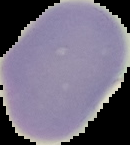
Summary:
  - Malaria status: uninfected
  - Image type: segmented cell region on a black background
  - Image size: 130×145 pixels
  - Preparation: thin blood film